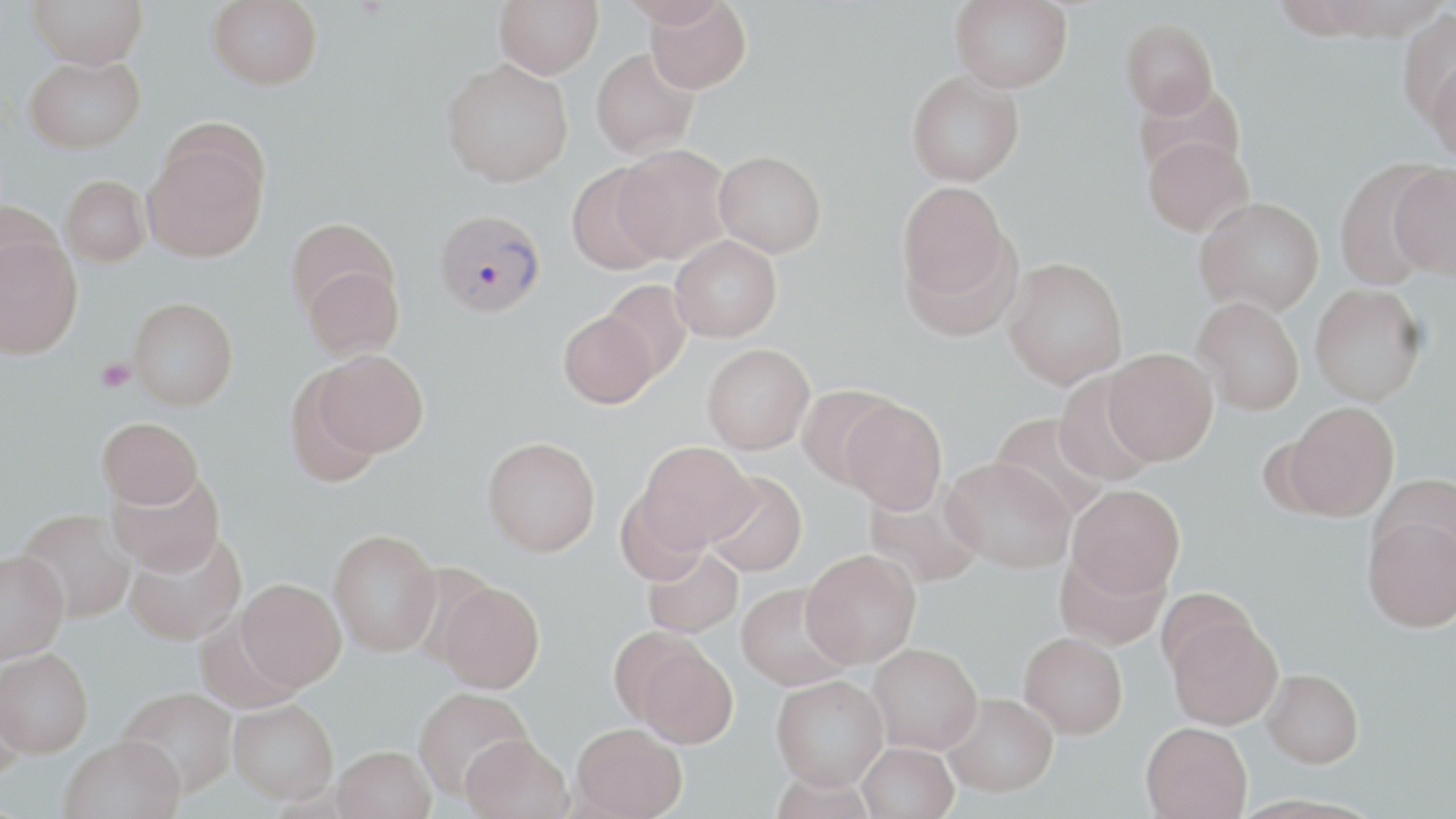

Summary:
  - Coordinate format: approximate bounding boxes as (x1, y1, x2, y2) in pixels
  - Platelet locations: (95, 358, 136, 392)
  - Plasmodium vivax-infected red blood cell locations: (434, 208, 546, 319)
  - Uninfected red blood cell locations: (27, 0, 147, 69), (207, 0, 322, 90), (494, 0, 603, 78), (619, 0, 731, 27), (644, 0, 752, 94), (950, 0, 1073, 92), (1397, 7, 1456, 125), (1121, 18, 1218, 118), (590, 48, 699, 159), (23, 55, 145, 153), (1426, 57, 1456, 168), (441, 58, 573, 187), (906, 70, 1024, 186), (1132, 81, 1246, 182), (142, 132, 269, 261), (1143, 135, 1253, 237), (614, 144, 733, 264), (714, 151, 826, 257), (1332, 158, 1445, 289), (566, 162, 671, 275), (1389, 164, 1456, 281), (59, 175, 150, 268), (896, 180, 1013, 308), (1195, 196, 1324, 315), (0, 198, 62, 297), (285, 217, 398, 320), (0, 235, 83, 359), (670, 235, 782, 342), (1002, 257, 1127, 389), (302, 265, 404, 361), (599, 280, 692, 382), (1310, 284, 1427, 406), (128, 297, 238, 410), (1193, 297, 1305, 415), (558, 311, 658, 408), (702, 343, 815, 454), (1103, 347, 1218, 465), (313, 349, 428, 456), (284, 372, 385, 489), (1053, 374, 1160, 484), (796, 384, 900, 487), (839, 398, 947, 514), (1284, 401, 1399, 520), (990, 413, 1110, 521), (97, 417, 203, 509), (482, 436, 601, 556), (636, 441, 757, 551), (940, 456, 1075, 573), (106, 470, 224, 577), (703, 471, 807, 577), (1369, 474, 1456, 572), (863, 483, 985, 586), (1067, 484, 1185, 599), (615, 488, 712, 585), (15, 509, 137, 624), (1362, 514, 1456, 633), (123, 529, 246, 645), (328, 529, 442, 656), (643, 546, 744, 637), (801, 548, 921, 667), (1054, 549, 1170, 650), (0, 550, 70, 663), (235, 578, 346, 691), (434, 581, 544, 694), (736, 582, 854, 690), (1164, 609, 1284, 730), (1019, 632, 1128, 738), (625, 635, 739, 748), (868, 642, 983, 753), (0, 648, 93, 757), (1262, 668, 1364, 767), (771, 674, 889, 790), (0, 684, 27, 781), (116, 686, 238, 796), (414, 687, 534, 798), (942, 693, 1058, 796), (229, 699, 338, 803), (1141, 721, 1253, 818), (571, 722, 688, 819), (460, 733, 573, 819), (59, 734, 184, 819), (858, 742, 959, 819), (332, 745, 435, 819)
  - Slide-level diagnosis: Plasmodium vivax
  - Stain: May-Grünwald-Giemsa
  - Image size: 1456×819 pixels
  - Field of view: one of a larger specimen
  - Magnification: 1000x
  - Preparation: thin blood smear
  - Modality: optical microscopy